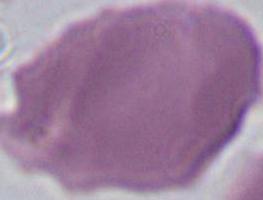 Photomicrograph. 1000x magnification. An erythrocyte is seen.